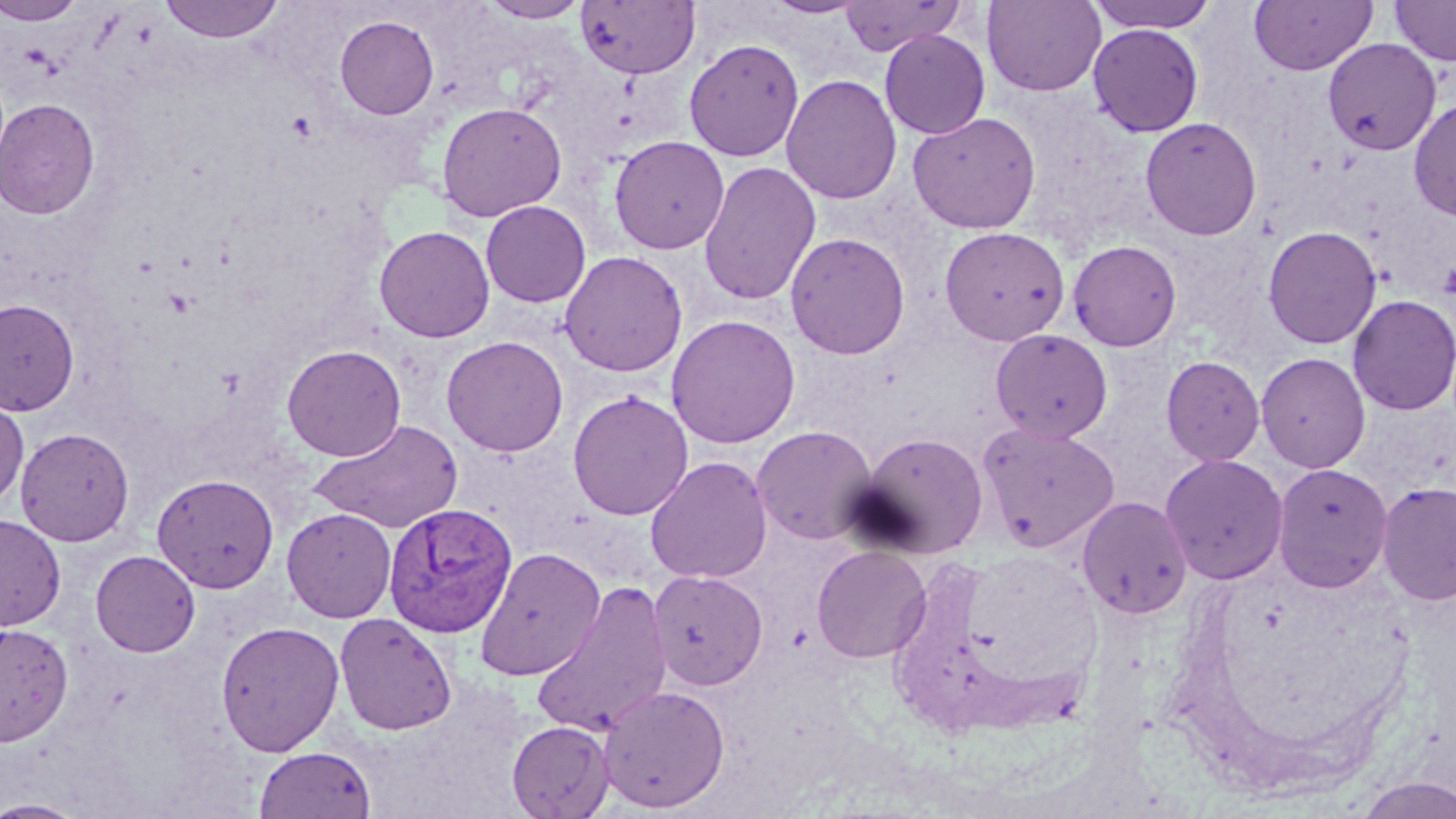

slide-level diagnosis = Plasmodium vivax
field of view = single
modality = light microscopy
Plasmodium vivax-infected red blood cell locations = approximate bounding boxes as named x1/y1/x2/y2 corners in pixels: (x1=383, y1=502, x2=517, y2=637)
preparation = thin blood smear
platelet locations = approximate bounding boxes as named x1/y1/x2/y2 corners in pixels: (x1=1438, y1=261, x2=1456, y2=302)
image size = 1456×819 pixels
stain = May-Grünwald-Giemsa
magnification = 1000x
uninfected red blood cell locations = approximate bounding boxes as named x1/y1/x2/y2 corners in pixels: (x1=159, y1=0, x2=284, y2=43), (x1=481, y1=0, x2=590, y2=23), (x1=763, y1=0, x2=870, y2=18), (x1=839, y1=0, x2=967, y2=55), (x1=982, y1=0, x2=1106, y2=96), (x1=1086, y1=0, x2=1221, y2=33), (x1=1249, y1=0, x2=1378, y2=76), (x1=1389, y1=0, x2=1456, y2=66), (x1=0, y1=1, x2=86, y2=25), (x1=575, y1=1, x2=700, y2=79), (x1=335, y1=15, x2=439, y2=120), (x1=1087, y1=24, x2=1204, y2=137), (x1=879, y1=29, x2=990, y2=139), (x1=1322, y1=38, x2=1442, y2=156), (x1=684, y1=39, x2=804, y2=161), (x1=781, y1=74, x2=902, y2=205), (x1=1408, y1=97, x2=1456, y2=222), (x1=0, y1=98, x2=101, y2=219), (x1=436, y1=101, x2=567, y2=222), (x1=908, y1=111, x2=1041, y2=234), (x1=1140, y1=117, x2=1262, y2=240), (x1=608, y1=135, x2=730, y2=254), (x1=698, y1=160, x2=821, y2=305), (x1=480, y1=200, x2=591, y2=307), (x1=374, y1=225, x2=495, y2=342), (x1=1263, y1=225, x2=1382, y2=349), (x1=939, y1=226, x2=1070, y2=346), (x1=785, y1=232, x2=910, y2=360), (x1=1067, y1=239, x2=1182, y2=351), (x1=559, y1=250, x2=687, y2=376), (x1=1348, y1=295, x2=1456, y2=416), (x1=0, y1=298, x2=80, y2=416), (x1=665, y1=314, x2=801, y2=449), (x1=990, y1=328, x2=1113, y2=443), (x1=441, y1=335, x2=568, y2=456), (x1=282, y1=344, x2=406, y2=461), (x1=1255, y1=352, x2=1371, y2=473), (x1=1161, y1=355, x2=1265, y2=466), (x1=568, y1=389, x2=693, y2=520), (x1=0, y1=397, x2=28, y2=509), (x1=308, y1=418, x2=465, y2=533), (x1=977, y1=421, x2=1120, y2=552), (x1=752, y1=425, x2=879, y2=545), (x1=15, y1=427, x2=135, y2=546), (x1=854, y1=431, x2=990, y2=558), (x1=1160, y1=453, x2=1289, y2=585), (x1=645, y1=456, x2=773, y2=583), (x1=1272, y1=462, x2=1393, y2=593), (x1=152, y1=473, x2=279, y2=592), (x1=1377, y1=480, x2=1456, y2=607), (x1=1076, y1=495, x2=1194, y2=619), (x1=282, y1=507, x2=397, y2=622), (x1=0, y1=515, x2=66, y2=630), (x1=811, y1=545, x2=932, y2=663), (x1=475, y1=547, x2=606, y2=681), (x1=90, y1=550, x2=200, y2=657), (x1=649, y1=571, x2=768, y2=690), (x1=531, y1=580, x2=674, y2=739), (x1=334, y1=613, x2=457, y2=735), (x1=215, y1=621, x2=345, y2=755), (x1=0, y1=623, x2=74, y2=746), (x1=597, y1=685, x2=730, y2=813), (x1=507, y1=720, x2=614, y2=818), (x1=253, y1=746, x2=376, y2=819), (x1=1353, y1=776, x2=1456, y2=818), (x1=0, y1=798, x2=91, y2=818)